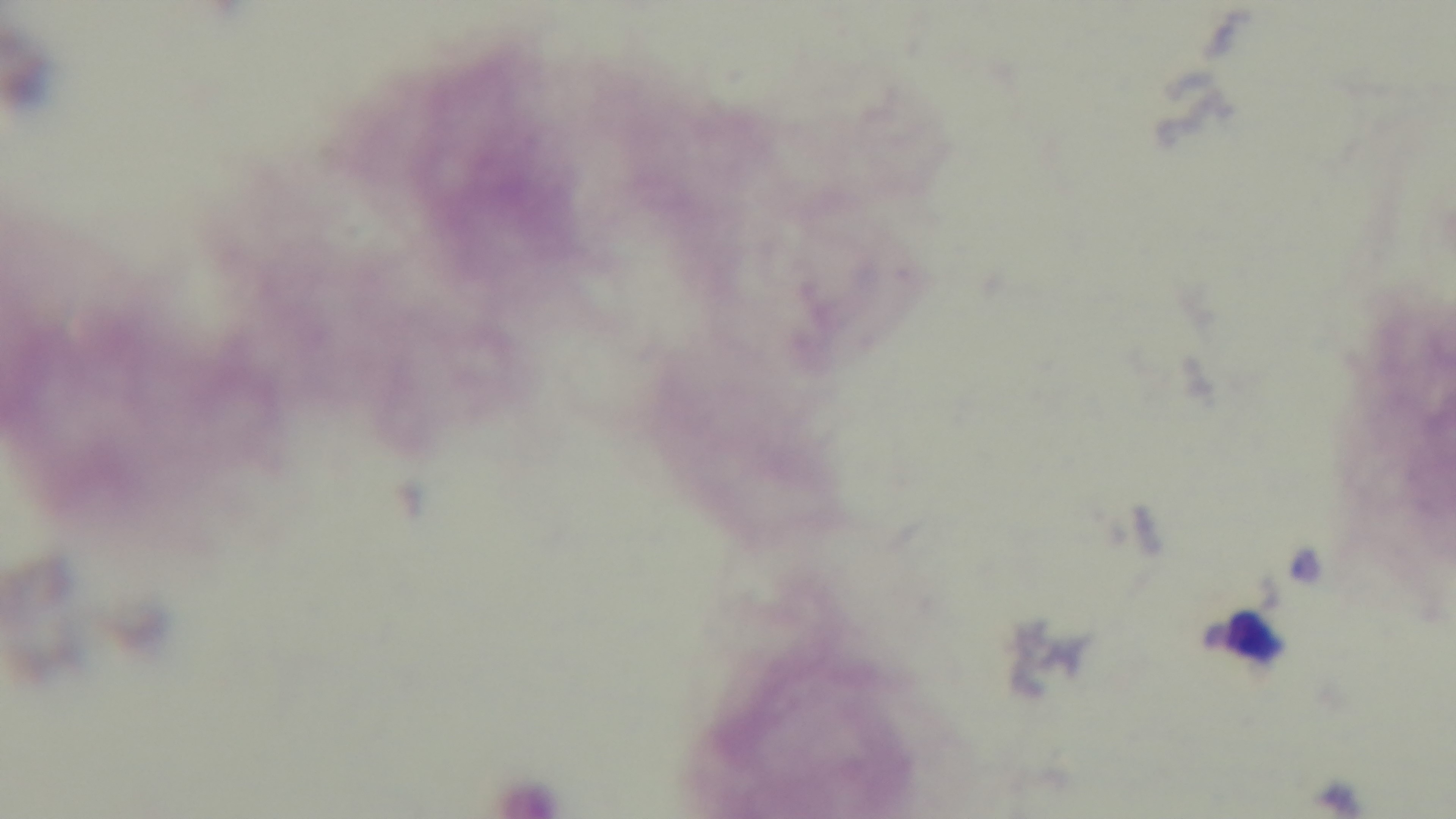 Mounted 4K digital camera. Giemsa stain. Preparation: thick smear. Photomicrograph. One field from the slide. Oil-immersion objective, 100x. Malaria status: negative.